Report the malaria status of this cell.
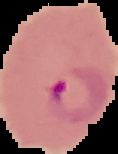

It is parasitized.

Summary:
  - Image size: 118×154 pixels
  - Image type: segmented cell region with the area outside set to black
  - Preparation: thin blood film